Assess this cell for malaria.
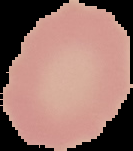

It is uninfected.

image type = cell region segmented out of the field of view; surrounding area masked to black
preparation = thin blood smear
image size = 133×151 pixels